Assess this cell for malaria.
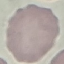
It is uninfected.

Acquired by smartphone through the microscope eyepiece. Thin smear of blood. Cell patch, automatically extracted from a larger field of view and resized to 64 × 64 pixels. Giemsa-stained preparation.